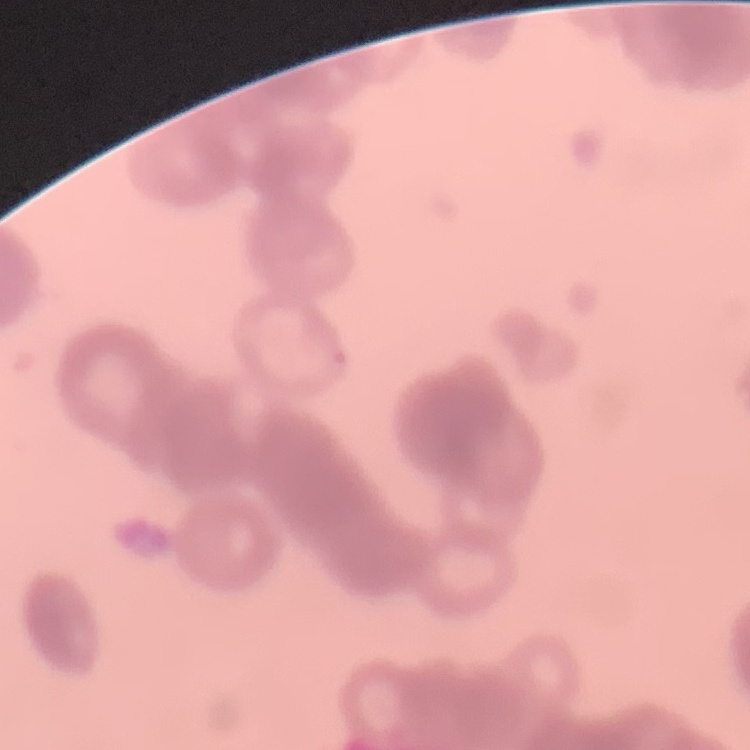
The red blood cells exhibit rouleaux formation. Stained with either Field's or Giemsa. One tile cut from a larger photomicrograph. Thin peripheral smear.